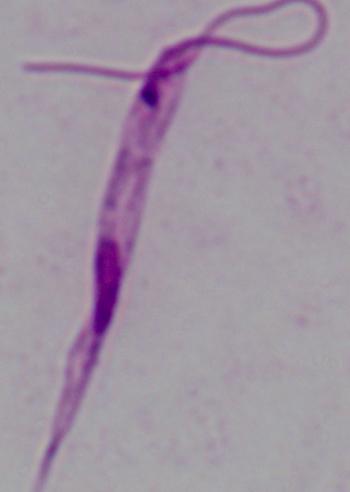 A Leishmania parasite is seen. 1000x magnification. Photomicrograph.